Describe the morphology of the red blood cells.
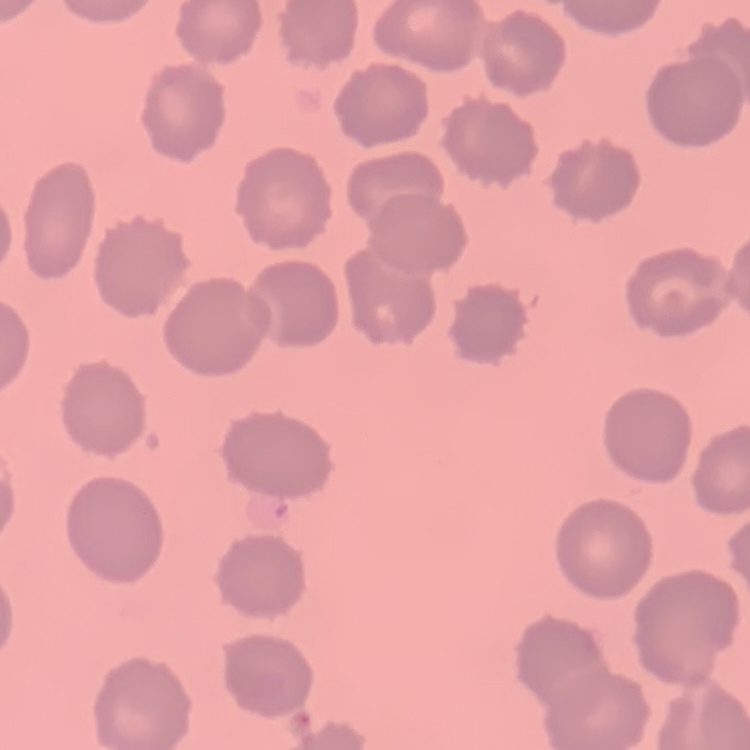
They show no rouleaux formation.

Summary:
  - Stain: Field's or Giemsa
  - Image type: square crop of a larger photomicrograph
  - Preparation: thin blood film